Comment on the morphology of the red blood cells.
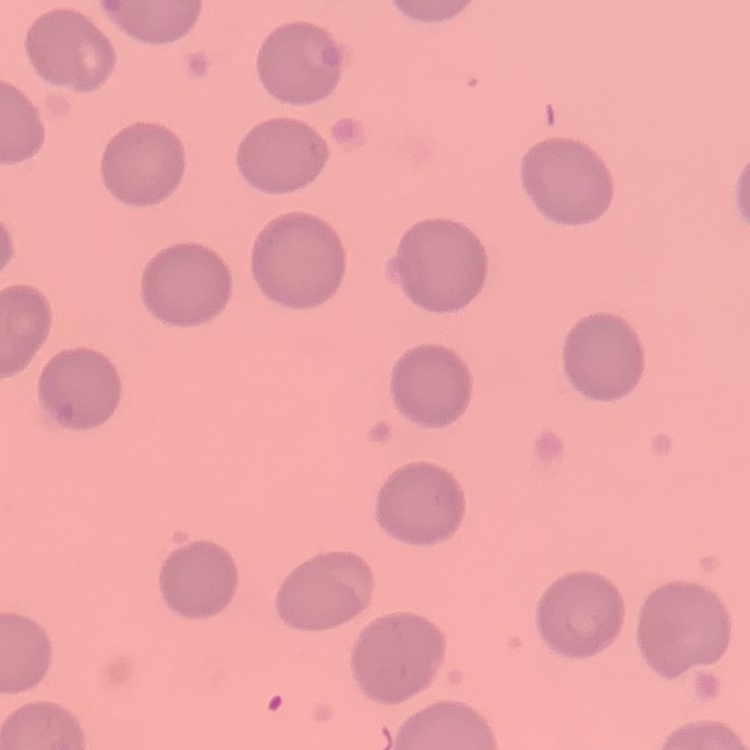
They show no rouleaux formation.

image_type: one tile cut from a larger photomicrograph
preparation: thin blood smear
stain: Field's or Giemsa